Describe the morphology of the erythrocytes.
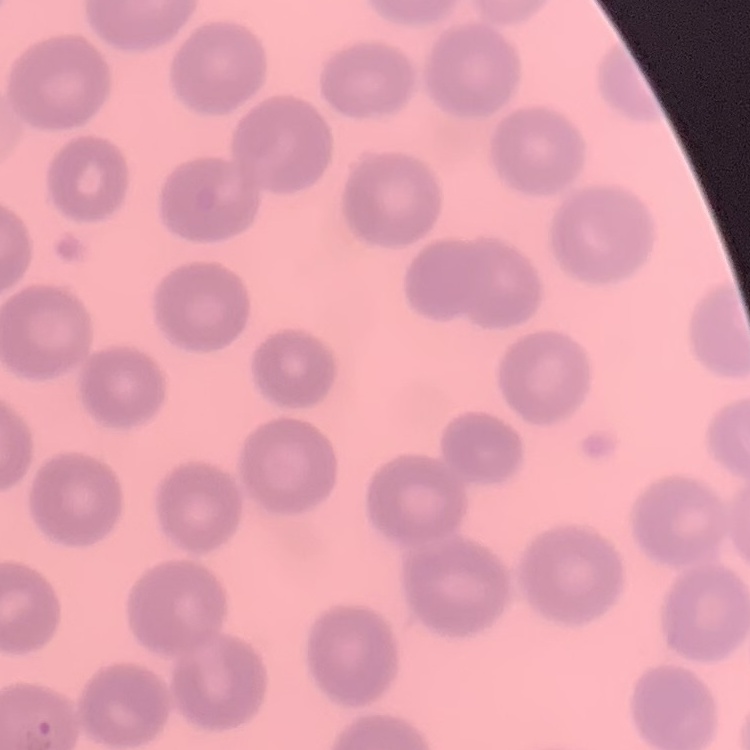
They show no rouleaux formation.

Square crop of a larger photomicrograph. Field's or Giemsa stain. Thin peripheral smear.